Report the malaria status of this cell.
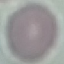

It is uninfected.

image type = cell patch, automatically extracted from a larger field of view and resized to 64 × 64 pixels
capture = smartphone through the microscope eyepiece
stain = Giemsa
preparation = thin blood film